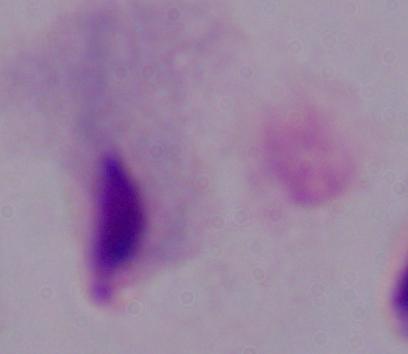
magnification = 1000x
modality = micrograph
identification = trichomonad